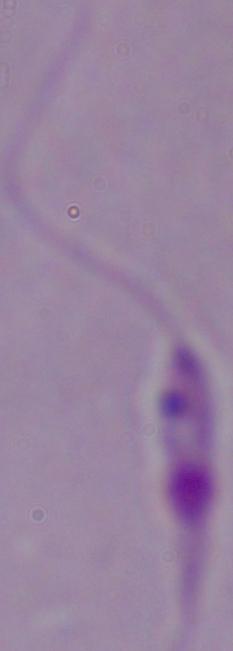

magnification = 1000x
modality = photomicrograph
identification = Leishmania